Name the cell type shown.
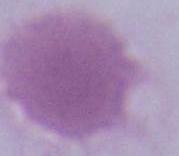

This is an erythrocyte.

{
  "magnification": "1000x",
  "modality": "photomicrograph"
}